Give the position of every Plasmodium parasite.
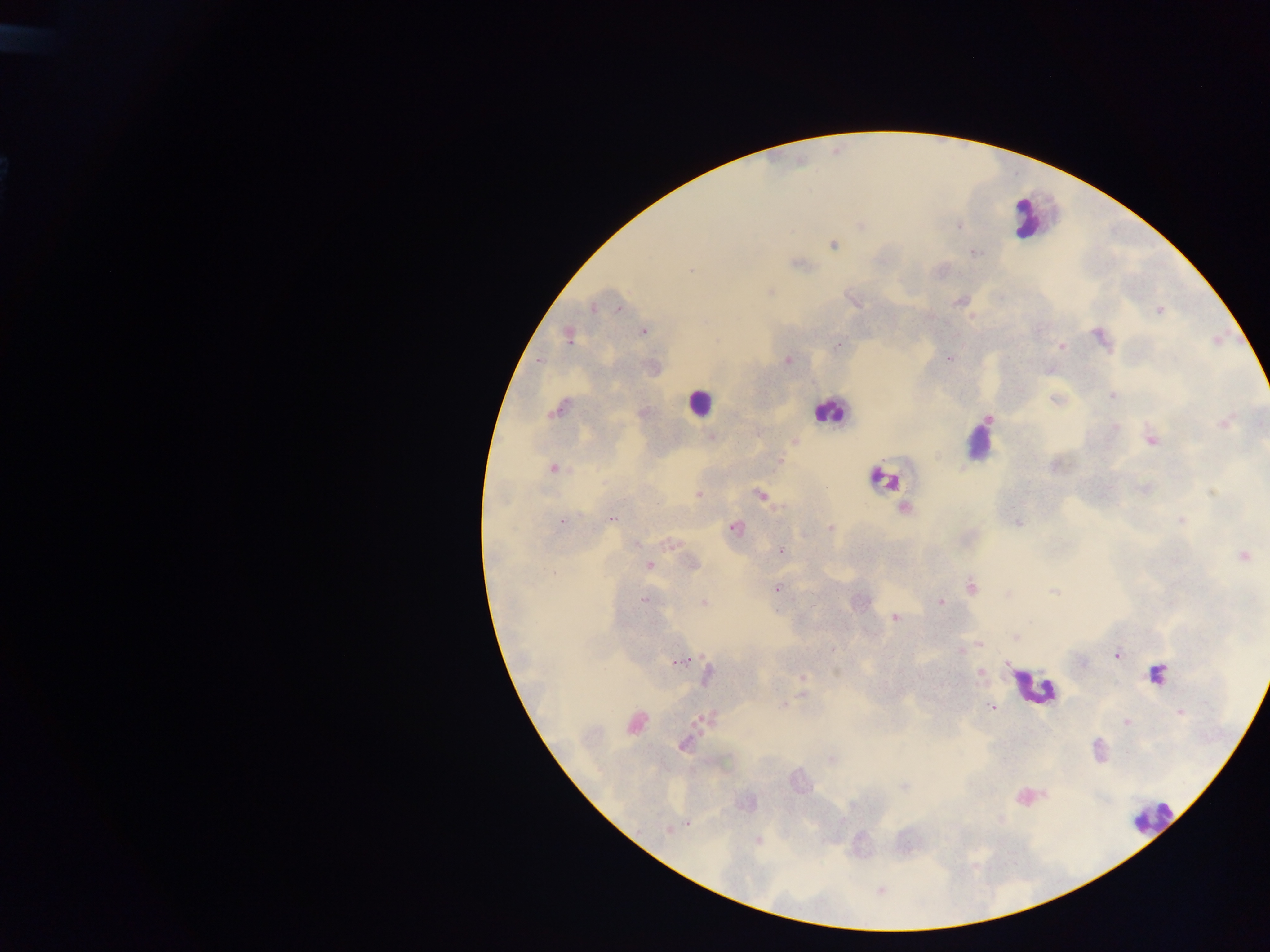
Approximate centers as (x, y) in pixels.
Plasmodium parasites: (959, 227), (833, 244), (974, 253), (690, 270), (770, 292), (855, 302), (958, 302), (619, 307), (593, 309), (1159, 311), (644, 332), (569, 337), (1100, 337), (839, 345), (1061, 346), (949, 358), (540, 361), (788, 361), (1112, 395), (1055, 399), (558, 409), (988, 419), (1224, 423), (1116, 427), (712, 436), (1151, 439), (795, 441), (779, 461), (553, 468), (1212, 493), (699, 494), (760, 494), (904, 509), (612, 518), (562, 521), (1181, 521), (1017, 523), (734, 528), (830, 528), (636, 543), (670, 544), (781, 552), (1243, 556), (692, 563), (649, 565), (972, 587), (776, 589), (1054, 590), (1008, 594), (643, 600), (704, 603), (941, 603), (813, 605), (895, 618), (1029, 622), (1016, 638), (979, 644), (961, 651), (1117, 654), (680, 661), (1083, 663), (1006, 666), (980, 674), (706, 675), (803, 679), (802, 695), (782, 704), (992, 707), (1180, 712), (708, 718), (1126, 722), (636, 723), (684, 744), (1098, 747), (831, 760), (904, 787), (687, 824), (668, 831), (757, 841).
One object is labeled both Plasmodium parasite and leukocyte by the source: (883, 478).

Leukocyte locations: (1024, 216), (697, 402), (829, 410), (978, 447), (1154, 675), (1033, 687), (1151, 818). Collected in Ghana. Single field of view. Mobile-phone photograph taken through the microscope. Thick blood smear. Image is 1270×952 pixels.